Report the malaria status of this cell.
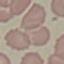

Uninfected.

Summary:
  - Image type: cell patch, automatically extracted from a larger field of view and resized to 64 × 64 pixels
  - Preparation: thin blood film
  - Capture: smartphone camera at the microscope eyepiece
  - Stain: Giemsa